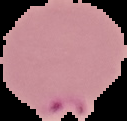

Summary:
  - Image type: segmented cell region with the area outside set to black
  - Malaria status: parasitized
  - Preparation: thin blood smear
  - Image size: 127×121 pixels